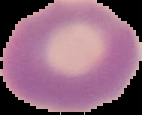 The area outside the segmented cell region is set to black. From a thin blood film. Result: negative for Plasmodium parasites. Image is 142×115 pixels.